Outline each blood parasite and name the species.
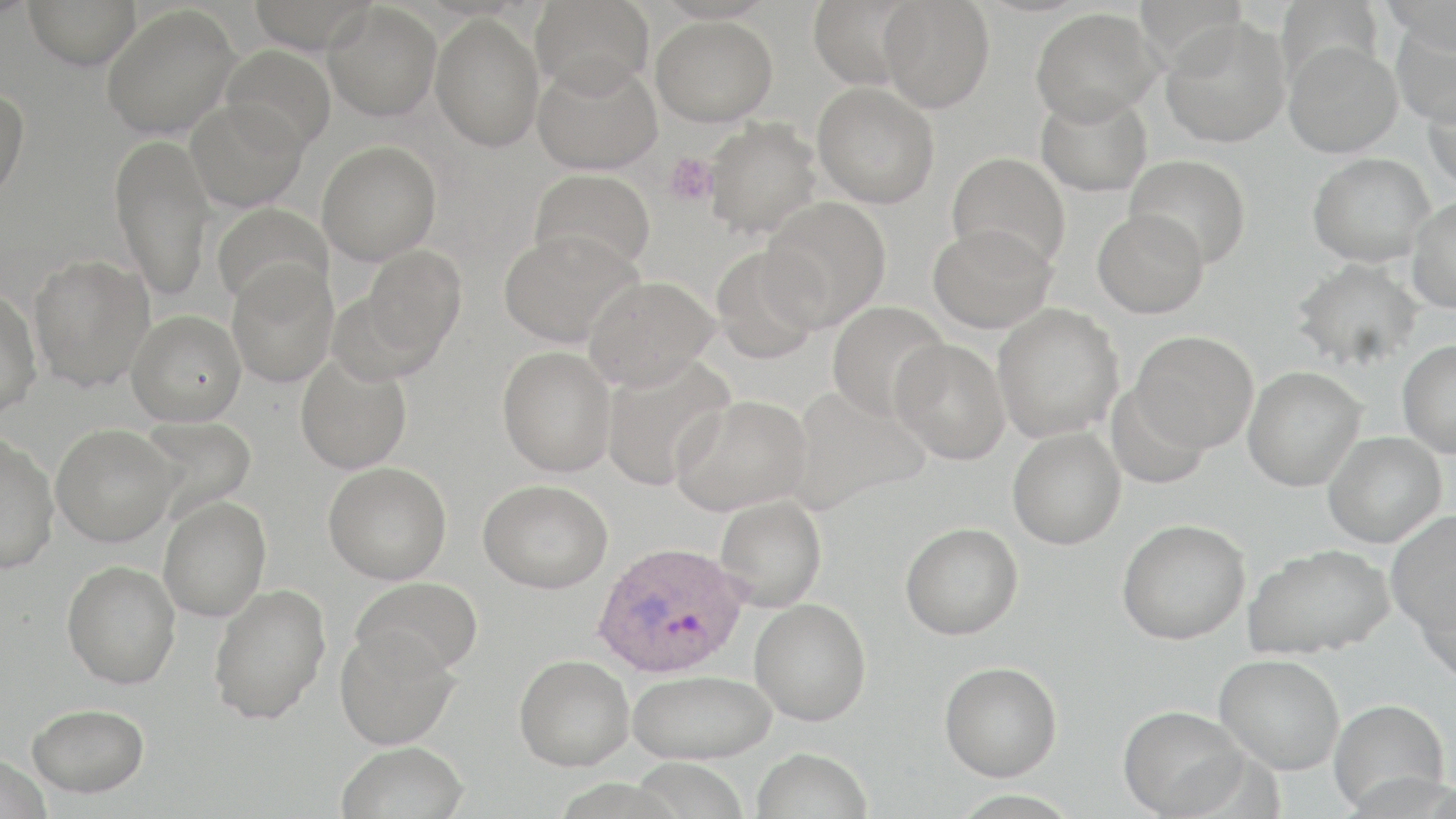
Approximate bounding boxes as named x1/y1/x2/y2 corners in pixels.
Plasmodium ovale-infected red blood cells: (x1=592, y1=540, x2=749, y2=678).
No Plasmodium falciparum, Plasmodium malariae, Plasmodium vivax, Babesia divergens, or Trypanosoma brucei observed.

Platelet locations: (x1=662, y1=152, x2=718, y2=207). Uninfected red blood cell locations: (x1=23, y1=0, x2=142, y2=69), (x1=248, y1=0, x2=378, y2=54), (x1=530, y1=0, x2=654, y2=97), (x1=1133, y1=0, x2=1251, y2=70), (x1=1275, y1=0, x2=1385, y2=90), (x1=1380, y1=0, x2=1455, y2=50), (x1=807, y1=1, x2=924, y2=89), (x1=878, y1=1, x2=995, y2=113), (x1=322, y1=2, x2=441, y2=121), (x1=101, y1=4, x2=240, y2=141), (x1=1029, y1=7, x2=1163, y2=125), (x1=430, y1=14, x2=544, y2=151), (x1=651, y1=15, x2=778, y2=127), (x1=1390, y1=15, x2=1456, y2=129), (x1=1159, y1=18, x2=1291, y2=148), (x1=1283, y1=40, x2=1402, y2=157), (x1=221, y1=44, x2=336, y2=154), (x1=533, y1=59, x2=660, y2=174), (x1=812, y1=82, x2=940, y2=208), (x1=1422, y1=83, x2=1456, y2=194), (x1=0, y1=84, x2=30, y2=208), (x1=1034, y1=87, x2=1153, y2=197), (x1=186, y1=98, x2=308, y2=212), (x1=703, y1=117, x2=823, y2=238), (x1=110, y1=133, x2=216, y2=300), (x1=317, y1=140, x2=441, y2=265), (x1=946, y1=152, x2=1071, y2=270), (x1=1308, y1=153, x2=1435, y2=266), (x1=1125, y1=154, x2=1251, y2=267), (x1=529, y1=168, x2=656, y2=275), (x1=1407, y1=195, x2=1456, y2=313), (x1=761, y1=198, x2=891, y2=329), (x1=211, y1=202, x2=332, y2=312), (x1=1093, y1=208, x2=1209, y2=318), (x1=928, y1=223, x2=1057, y2=334), (x1=498, y1=230, x2=642, y2=348), (x1=709, y1=244, x2=824, y2=364), (x1=360, y1=245, x2=466, y2=359), (x1=28, y1=253, x2=155, y2=392), (x1=1291, y1=258, x2=1424, y2=371), (x1=226, y1=263, x2=338, y2=387), (x1=583, y1=276, x2=718, y2=391), (x1=0, y1=286, x2=43, y2=419), (x1=326, y1=290, x2=440, y2=386), (x1=827, y1=300, x2=950, y2=422), (x1=992, y1=303, x2=1124, y2=443), (x1=126, y1=309, x2=246, y2=426), (x1=1131, y1=331, x2=1259, y2=453), (x1=890, y1=339, x2=1011, y2=465), (x1=1397, y1=340, x2=1456, y2=457), (x1=497, y1=346, x2=616, y2=477), (x1=295, y1=352, x2=412, y2=474), (x1=601, y1=356, x2=734, y2=490), (x1=1243, y1=366, x2=1366, y2=491), (x1=1106, y1=382, x2=1211, y2=490), (x1=789, y1=386, x2=930, y2=511), (x1=671, y1=394, x2=812, y2=516), (x1=140, y1=414, x2=256, y2=515), (x1=50, y1=424, x2=181, y2=547), (x1=1007, y1=427, x2=1126, y2=549), (x1=1322, y1=431, x2=1446, y2=548), (x1=0, y1=432, x2=59, y2=573), (x1=323, y1=461, x2=452, y2=584), (x1=478, y1=479, x2=613, y2=593), (x1=714, y1=495, x2=827, y2=612), (x1=158, y1=496, x2=271, y2=622), (x1=1386, y1=512, x2=1456, y2=637), (x1=1117, y1=519, x2=1250, y2=644), (x1=900, y1=522, x2=1023, y2=639), (x1=1242, y1=543, x2=1395, y2=660), (x1=62, y1=560, x2=181, y2=688), (x1=350, y1=577, x2=484, y2=677), (x1=1415, y1=577, x2=1456, y2=686), (x1=208, y1=583, x2=331, y2=724), (x1=749, y1=599, x2=871, y2=726), (x1=334, y1=628, x2=460, y2=749), (x1=514, y1=653, x2=635, y2=771), (x1=1215, y1=653, x2=1345, y2=774), (x1=939, y1=661, x2=1062, y2=781), (x1=627, y1=669, x2=777, y2=765), (x1=1328, y1=698, x2=1451, y2=815), (x1=27, y1=703, x2=149, y2=797), (x1=1117, y1=704, x2=1251, y2=818), (x1=335, y1=741, x2=469, y2=819), (x1=752, y1=747, x2=873, y2=819), (x1=0, y1=753, x2=52, y2=818), (x1=949, y1=789, x2=1083, y2=818). Slide-level diagnosis: Plasmodium ovale. 1000x magnification. Image is 1456×819 pixels. May-Grünwald-Giemsa stain. Single field of view. Thin blood smear. Optical microscopy.